State which cell type is depicted.
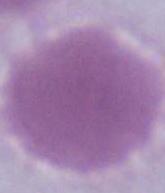
This is an erythrocyte.

modality = micrograph
magnification = 1000x